Name the parasite shown.
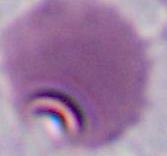

Plasmodium.

400x or 1000x magnification. Micrograph.